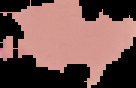 Result: no Plasmodium parasites seen. Image is 136×88 pixels. Segmented cell region on a black background. From a thin blood smear.